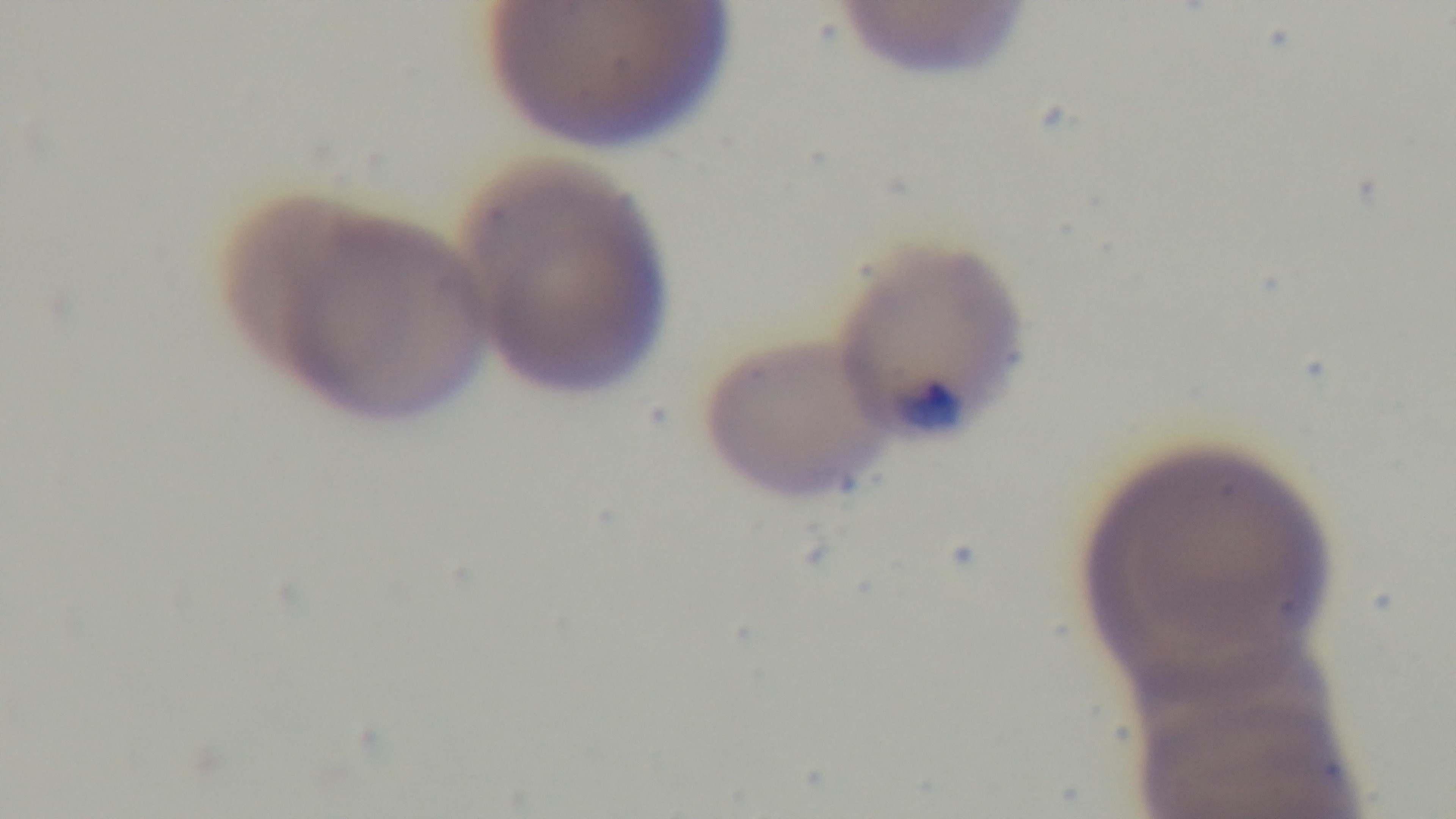
Giemsa-stained. 100x oil-immersion objective. One field from the slide. Malaria status: infected. Mounted 4K digital camera. Preparation: thin. Photomicrograph.